Outline each blood parasite and name the species.
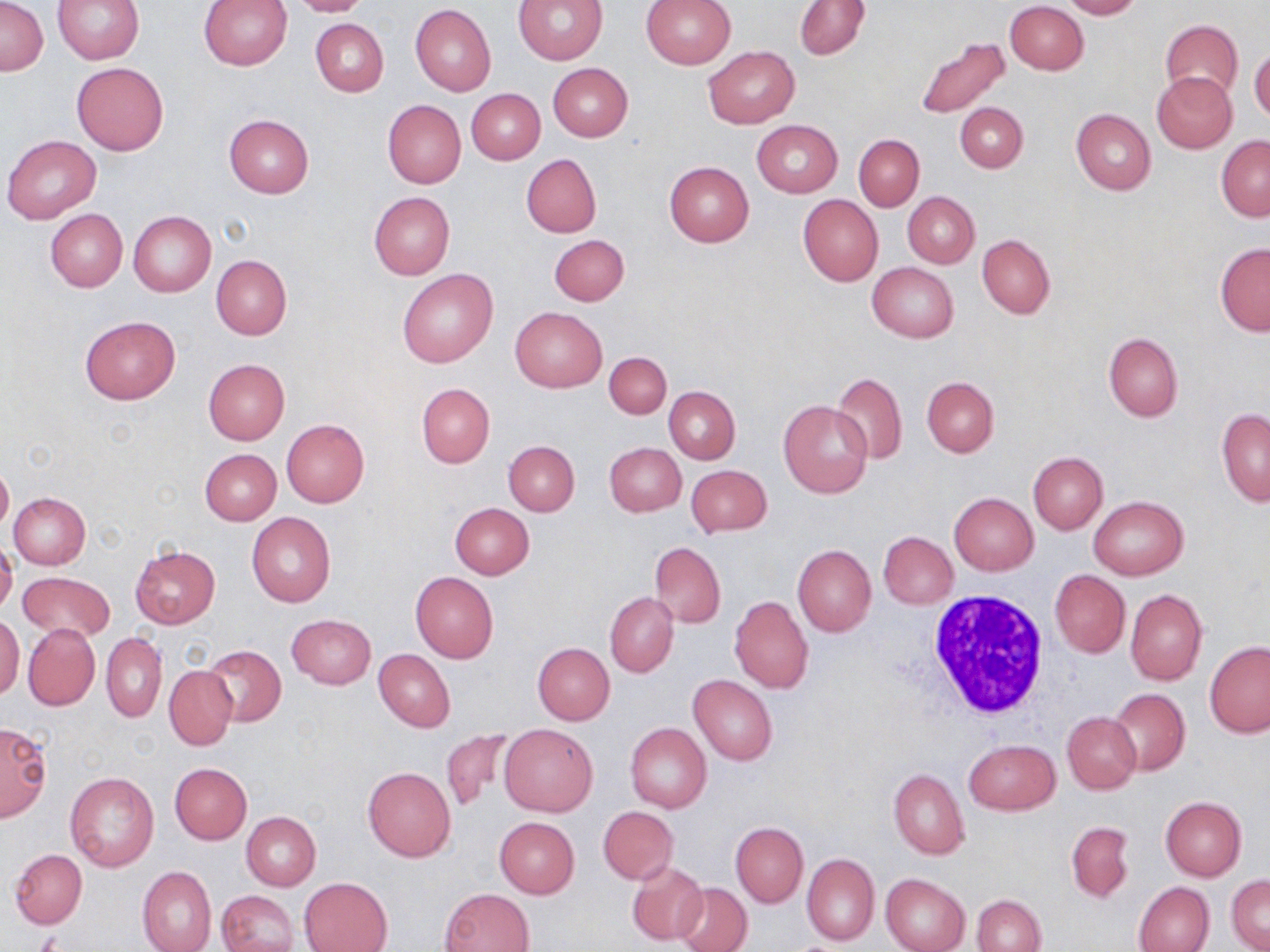

No blood parasites observed.

Approximate bounding boxes as (x1,y1)-(x2,y2) corner pairs in pixels. Uninfected red blood cell locations: (1,0)-(47,75), (52,0)-(144,64), (285,0)-(370,17), (513,0)-(606,65), (640,0)-(737,68), (1060,0)-(1143,19), (198,1)-(293,69), (795,1)-(868,59), (1006,2)-(1088,75), (410,4)-(496,97), (310,19)-(388,97), (1160,20)-(1244,103), (912,33)-(1012,120), (703,45)-(799,128), (1249,47)-(1270,121), (72,62)-(170,155), (547,63)-(633,141), (1151,72)-(1238,153), (466,89)-(544,164), (382,100)-(466,188), (954,102)-(1028,173), (1071,109)-(1156,194), (224,114)-(315,198), (752,119)-(842,196), (854,133)-(924,211), (2,134)-(102,225), (1216,136)-(1270,221), (520,153)-(601,238), (665,161)-(755,247), (902,191)-(980,269), (369,192)-(455,279), (798,194)-(883,286), (44,209)-(128,293), (128,211)-(216,296), (550,234)-(630,306), (978,235)-(1055,318), (1215,243)-(1270,334), (211,255)-(291,339), (867,263)-(959,343), (397,268)-(498,369), (510,307)-(606,391), (80,315)-(180,405), (1103,333)-(1183,422), (604,352)-(671,419), (203,359)-(289,444), (831,372)-(908,463), (921,376)-(999,456), (416,383)-(495,468), (664,386)-(740,464), (780,399)-(872,498), (1218,407)-(1270,506), (282,419)-(369,507), (504,441)-(579,516), (604,442)-(686,516), (200,449)-(282,524), (1027,451)-(1106,533), (0,460)-(13,533), (686,464)-(773,536), (9,492)-(91,569), (948,492)-(1038,575), (1088,495)-(1188,579), (449,502)-(535,578), (246,512)-(335,607), (877,531)-(957,609), (0,540)-(18,615), (650,542)-(726,628), (131,545)-(220,628), (793,545)-(876,636), (1049,569)-(1130,658), (17,571)-(115,642), (411,572)-(499,663), (1126,588)-(1208,687), (605,593)-(678,677), (729,595)-(813,693), (287,614)-(376,690), (0,615)-(23,699), (23,623)-(99,710), (101,632)-(166,722), (1205,642)-(1270,738), (533,643)-(614,725), (203,644)-(285,727), (374,649)-(455,732), (164,665)-(238,749), (689,675)-(778,766), (1109,688)-(1190,775), (1062,712)-(1141,793), (498,722)-(598,817), (625,722)-(712,812), (0,723)-(51,821), (440,727)-(518,811), (964,739)-(1060,815), (169,763)-(252,844), (362,766)-(456,861), (889,768)-(968,859), (65,772)-(160,872), (1160,796)-(1246,881), (598,807)-(677,884), (241,812)-(321,890), (494,817)-(579,899), (1065,820)-(1134,903), (730,821)-(808,907), (10,850)-(87,927), (802,853)-(879,947), (627,860)-(708,946), (138,866)-(216,952), (881,873)-(971,952), (1227,876)-(1269,952), (299,877)-(392,952), (673,881)-(753,952), (1133,881)-(1215,952), (441,888)-(535,952), (218,891)-(296,952), (973,894)-(1045,951). White blood cell locations: (924,589)-(1055,725). Slide-level diagnosis: no evidence of blood parasites. Image is 1270×952 pixels. Optical microscopy. May-Grünwald-Giemsa stain. Thin blood film. 1000x magnification. One field of a larger specimen.